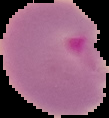
Summary:
  - Result: Plasmodium parasites detected
  - Preparation: thin blood film
  - Image size: 109×118 pixels
  - Image type: segmented cell region on a black background